Classify this cell by malaria status.
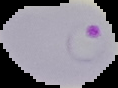
Parasitized.

Summary:
  - Preparation: thin blood film
  - Image type: segmented cell region on a black background
  - Image size: 118×88 pixels